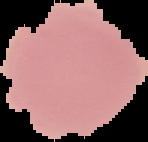
preparation: thin blood film
result: negative for malaria parasites
image_size: 148×142 pixels
image_type: cell region segmented out of the field of view; surrounding area masked to black